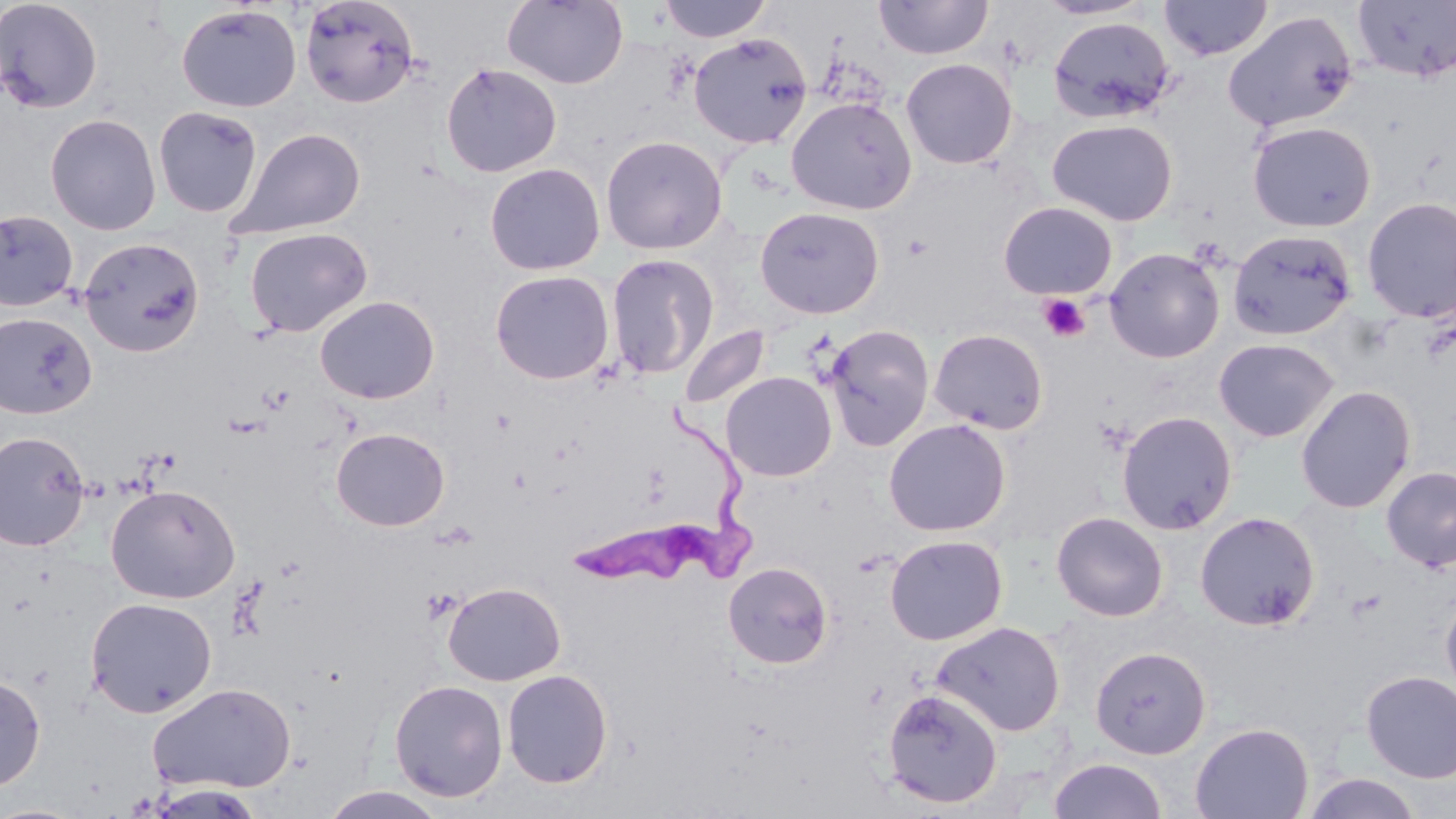
Approximate bounding boxes as named x1/y1/x2/y2 corners in pixels. Trypanosoma brucei locations: (x1=567, y1=396, x2=765, y2=591). Uninfected red blood cell locations: (x1=0, y1=0, x2=104, y2=114), (x1=502, y1=0, x2=628, y2=90), (x1=659, y1=0, x2=771, y2=43), (x1=1035, y1=0, x2=1155, y2=21), (x1=1159, y1=0, x2=1272, y2=61), (x1=299, y1=1, x2=421, y2=108), (x1=874, y1=1, x2=993, y2=60), (x1=1351, y1=2, x2=1456, y2=83), (x1=176, y1=3, x2=302, y2=113), (x1=1223, y1=9, x2=1358, y2=133), (x1=1047, y1=17, x2=1175, y2=123), (x1=688, y1=32, x2=812, y2=149), (x1=901, y1=58, x2=1018, y2=169), (x1=441, y1=62, x2=562, y2=178), (x1=786, y1=96, x2=917, y2=214), (x1=153, y1=106, x2=263, y2=217), (x1=44, y1=113, x2=162, y2=235), (x1=1047, y1=119, x2=1177, y2=226), (x1=1247, y1=120, x2=1376, y2=232), (x1=226, y1=126, x2=366, y2=240), (x1=601, y1=135, x2=728, y2=254), (x1=485, y1=162, x2=605, y2=275), (x1=1361, y1=196, x2=1456, y2=323), (x1=998, y1=201, x2=1118, y2=299), (x1=754, y1=206, x2=884, y2=319), (x1=0, y1=208, x2=79, y2=312), (x1=244, y1=227, x2=372, y2=337), (x1=1227, y1=229, x2=1356, y2=341), (x1=79, y1=237, x2=204, y2=357), (x1=1103, y1=247, x2=1225, y2=363), (x1=605, y1=254, x2=720, y2=380), (x1=490, y1=270, x2=614, y2=385), (x1=315, y1=296, x2=439, y2=404), (x1=0, y1=312, x2=97, y2=419), (x1=823, y1=324, x2=934, y2=451), (x1=679, y1=325, x2=770, y2=409), (x1=928, y1=328, x2=1048, y2=434), (x1=1213, y1=337, x2=1339, y2=443), (x1=721, y1=372, x2=837, y2=482), (x1=1295, y1=384, x2=1416, y2=513), (x1=1116, y1=411, x2=1238, y2=535), (x1=883, y1=418, x2=1011, y2=536), (x1=331, y1=427, x2=449, y2=531), (x1=0, y1=430, x2=91, y2=551), (x1=1381, y1=465, x2=1456, y2=572), (x1=105, y1=484, x2=240, y2=604), (x1=1051, y1=511, x2=1168, y2=622), (x1=1194, y1=511, x2=1320, y2=631), (x1=885, y1=534, x2=1008, y2=645), (x1=723, y1=561, x2=833, y2=668), (x1=443, y1=581, x2=566, y2=686), (x1=1440, y1=590, x2=1456, y2=705), (x1=85, y1=596, x2=217, y2=718), (x1=932, y1=621, x2=1066, y2=736), (x1=1090, y1=646, x2=1211, y2=759), (x1=502, y1=669, x2=613, y2=788), (x1=1360, y1=670, x2=1456, y2=783), (x1=0, y1=673, x2=46, y2=791), (x1=389, y1=679, x2=508, y2=802), (x1=148, y1=682, x2=296, y2=793), (x1=882, y1=688, x2=1003, y2=810), (x1=1190, y1=722, x2=1314, y2=819), (x1=1048, y1=758, x2=1168, y2=819), (x1=1300, y1=771, x2=1425, y2=818), (x1=146, y1=784, x2=265, y2=818), (x1=319, y1=787, x2=448, y2=819), (x1=0, y1=802, x2=87, y2=818). Platelet locations: (x1=1037, y1=293, x2=1091, y2=342), (x1=422, y1=589, x2=459, y2=623). Slide-level diagnosis: Trypanosoma brucei. May-Grünwald-Giemsa stain. 1000x magnification. Thin blood film. Light microscopy. Image is 1456×819 pixels. Single field of view.